Outline each white blood cell.
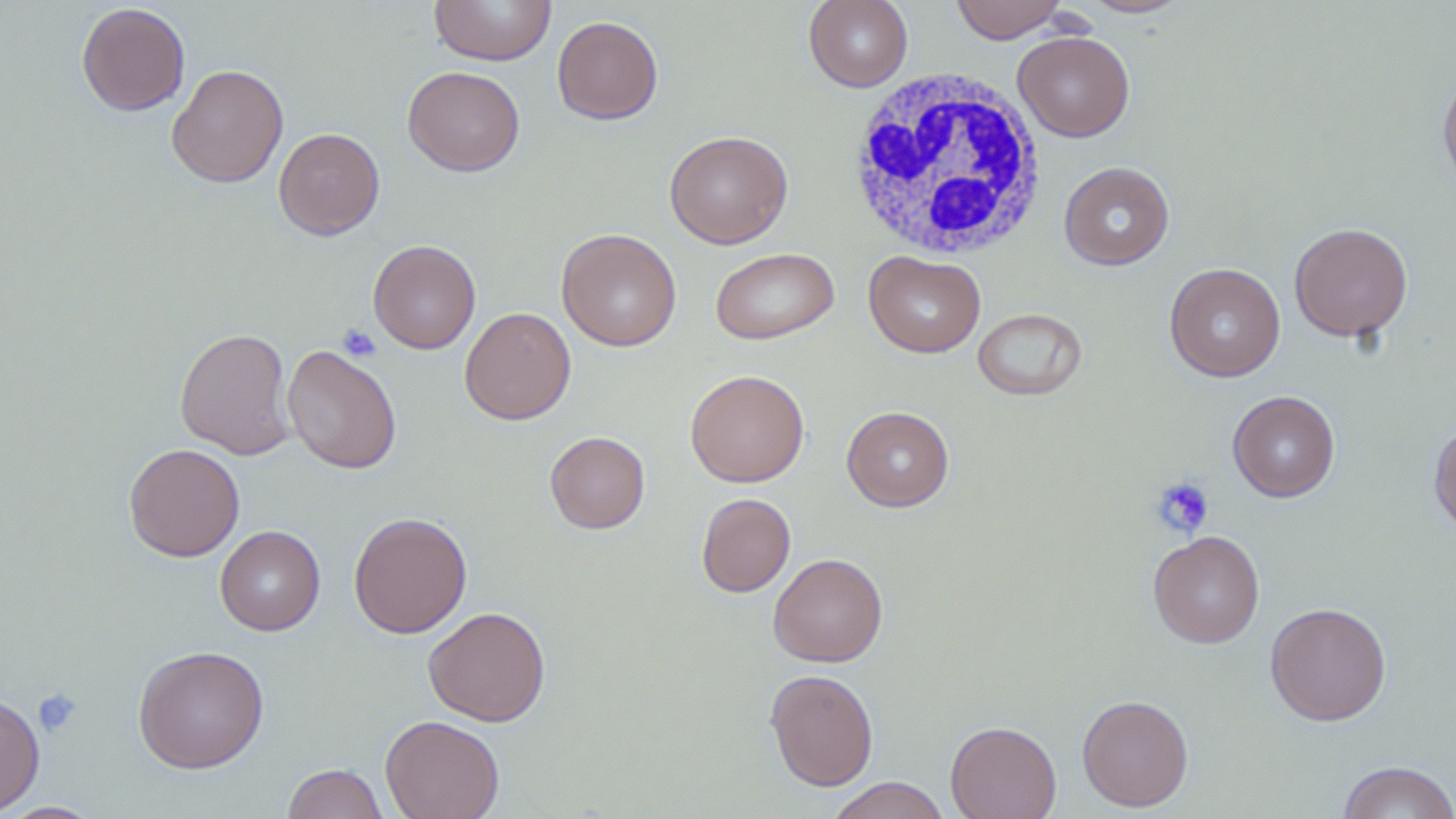
Approximate bounding boxes as named x1/y1/x2/y2 corners in pixels.
White blood cells: (x1=847, y1=67, x2=1049, y2=259).

Summary:
  - Platelet locations: (x1=338, y1=324, x2=381, y2=362), (x1=1151, y1=477, x2=1214, y2=538), (x1=32, y1=688, x2=83, y2=737)
  - Uninfected red blood cell locations: (x1=429, y1=0, x2=557, y2=66), (x1=803, y1=0, x2=913, y2=92), (x1=950, y1=0, x2=1068, y2=43), (x1=1079, y1=0, x2=1192, y2=18), (x1=77, y1=2, x2=191, y2=116), (x1=552, y1=16, x2=664, y2=124), (x1=1013, y1=31, x2=1135, y2=141), (x1=166, y1=64, x2=289, y2=188), (x1=402, y1=66, x2=525, y2=176), (x1=1438, y1=68, x2=1456, y2=193), (x1=273, y1=127, x2=385, y2=240), (x1=664, y1=130, x2=793, y2=249), (x1=1059, y1=161, x2=1175, y2=270), (x1=1289, y1=222, x2=1413, y2=342), (x1=556, y1=228, x2=682, y2=351), (x1=368, y1=239, x2=481, y2=354), (x1=710, y1=247, x2=839, y2=345), (x1=864, y1=251, x2=986, y2=358), (x1=1164, y1=262, x2=1285, y2=382), (x1=459, y1=306, x2=576, y2=425), (x1=973, y1=308, x2=1087, y2=401), (x1=175, y1=327, x2=296, y2=460), (x1=282, y1=344, x2=402, y2=474), (x1=685, y1=369, x2=810, y2=487), (x1=1227, y1=390, x2=1340, y2=502), (x1=841, y1=406, x2=955, y2=512), (x1=1428, y1=418, x2=1456, y2=537), (x1=545, y1=431, x2=650, y2=534), (x1=124, y1=443, x2=245, y2=562), (x1=696, y1=492, x2=796, y2=597), (x1=348, y1=512, x2=472, y2=638), (x1=215, y1=525, x2=325, y2=635), (x1=1148, y1=530, x2=1265, y2=648), (x1=768, y1=552, x2=888, y2=667), (x1=1264, y1=602, x2=1392, y2=726), (x1=423, y1=606, x2=551, y2=726), (x1=132, y1=645, x2=270, y2=773), (x1=764, y1=668, x2=879, y2=790), (x1=0, y1=693, x2=45, y2=817), (x1=1077, y1=695, x2=1194, y2=812), (x1=380, y1=714, x2=505, y2=819), (x1=946, y1=720, x2=1062, y2=819), (x1=1336, y1=760, x2=1456, y2=819), (x1=281, y1=763, x2=390, y2=819), (x1=825, y1=777, x2=951, y2=819), (x1=1, y1=802, x2=107, y2=818)
  - Slide-level diagnosis: negative for blood parasites
  - Image size: 1456×819 pixels
  - Modality: light microscopy
  - Field of view: single
  - Stain: May-Grünwald-Giemsa
  - Preparation: thin blood smear
  - Magnification: 1000x